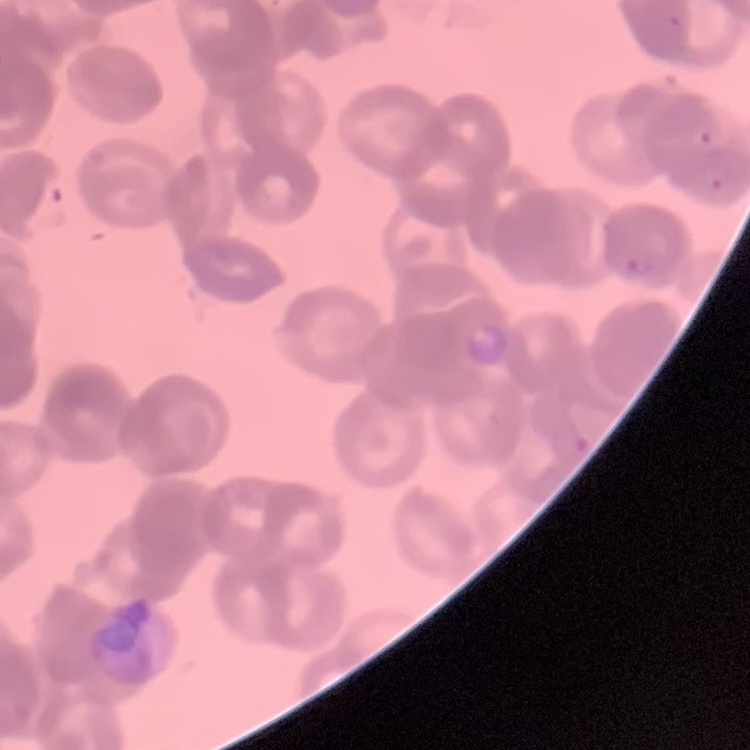

Summary:
  - Red blood cell morphology: rouleaux formation
  - Image type: square crop of a larger photomicrograph
  - Stain: Field's or Giemsa
  - Preparation: thin blood smear